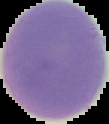
From a thin blood film. Malaria status: uninfected. Image is 109×124 pixels. The area outside the segmented cell region is set to black.